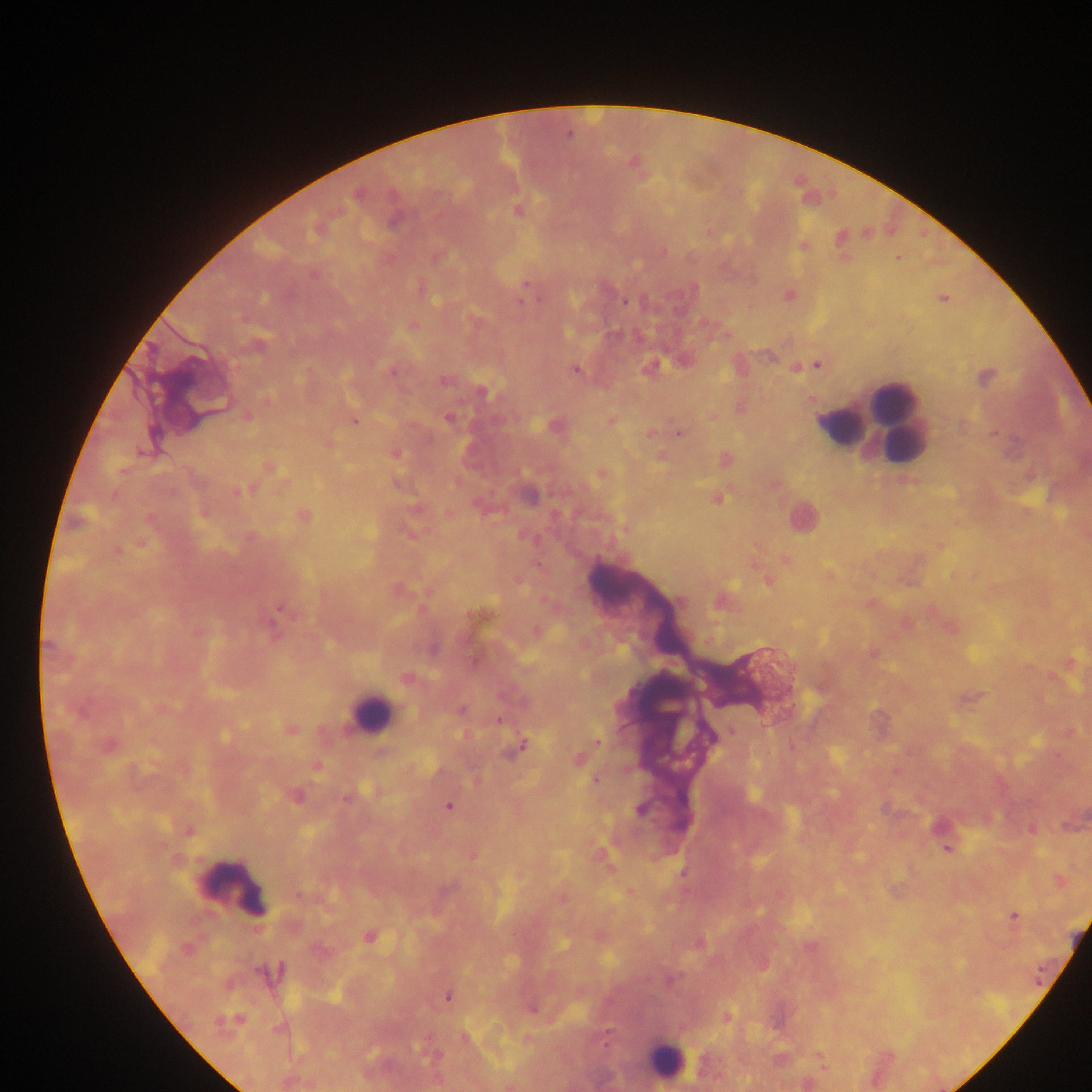

country = Ghana
leukocyte locations = approximate centers as (x, y) in pixels: (876, 429), (372, 713), (668, 1063)
field of view = single
capture = mobile-phone photograph through a microscope
image size = 1092×1092 pixels
preparation = thick blood film
malaria parasite locations = approximate centers as (x, y) in pixels: (897, 257), (312, 275), (524, 283), (519, 302), (624, 302), (413, 324), (816, 363), (575, 370), (392, 372), (354, 419), (448, 419), (993, 432), (678, 433), (281, 608), (500, 720), (598, 741), (524, 745), (595, 779), (448, 806), (947, 849), (1014, 915), (1040, 976), (446, 997)